Name the parasite shown.
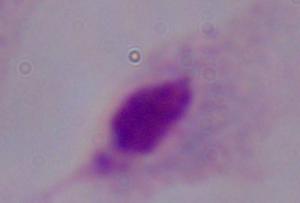
A trichomonad.

modality: photomicrograph
magnification: 1000x